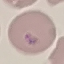

Summary:
  - Malaria status: uninfected
  - Image type: cell patch, automatically extracted from a larger field of view and resized to 64 × 64 pixels
  - Stain: Giemsa
  - Preparation: thin smear
  - Capture: smartphone camera at the microscope eyepiece